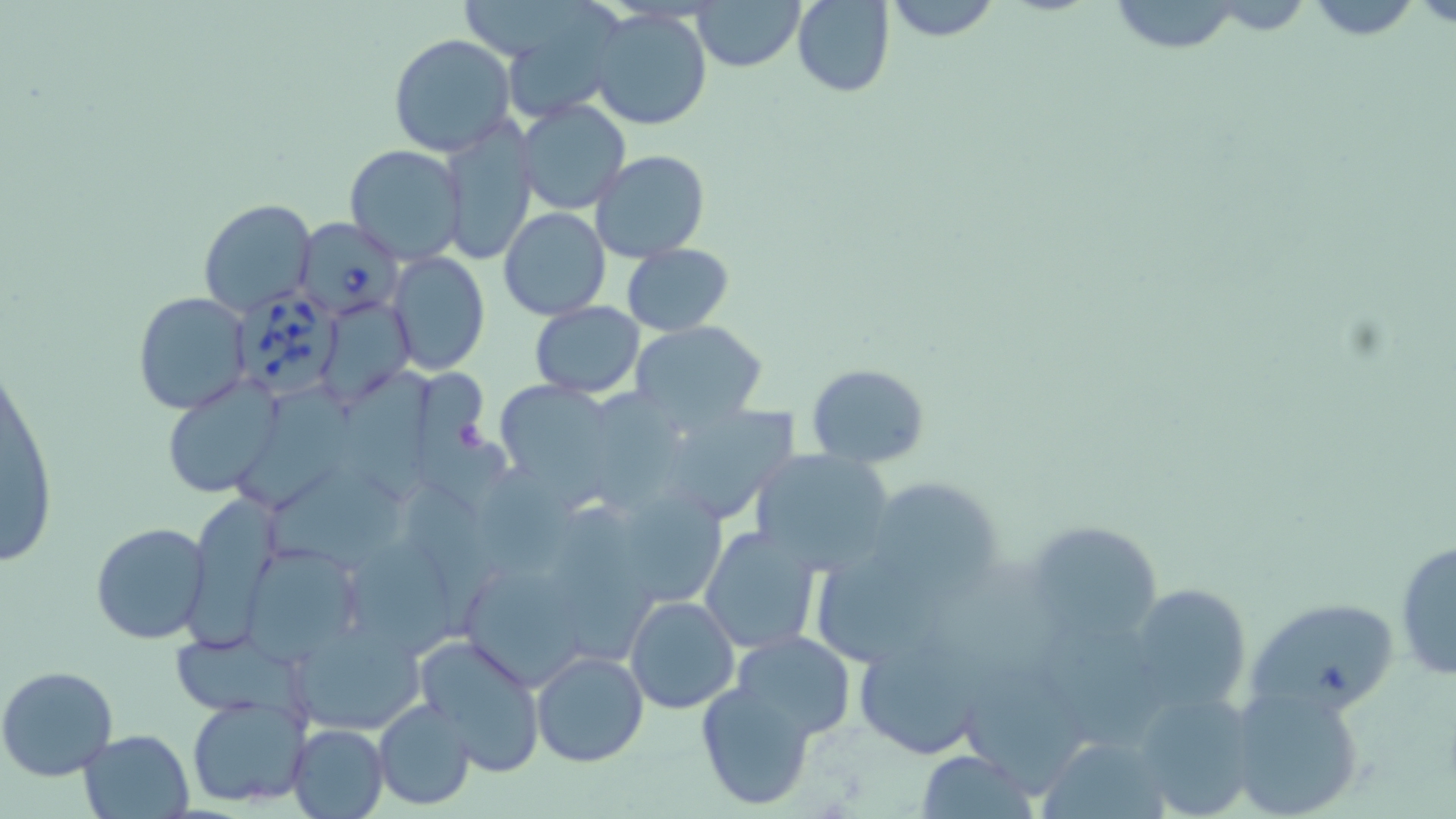
Approximate bounding boxes as named x1/y1/x2/y2 corners in pixels. Babesia divergens-infected red blood cell locations: (x1=297, y1=217, x2=404, y2=320), (x1=235, y1=287, x2=344, y2=400). Uninfected red blood cell locations: (x1=693, y1=0, x2=805, y2=71), (x1=793, y1=0, x2=895, y2=97), (x1=882, y1=0, x2=1000, y2=41), (x1=1104, y1=0, x2=1249, y2=56), (x1=1296, y1=0, x2=1438, y2=40), (x1=588, y1=7, x2=712, y2=131), (x1=515, y1=12, x2=628, y2=122), (x1=388, y1=34, x2=516, y2=157), (x1=516, y1=98, x2=632, y2=216), (x1=439, y1=117, x2=538, y2=267), (x1=345, y1=145, x2=466, y2=266), (x1=591, y1=150, x2=711, y2=261), (x1=198, y1=199, x2=317, y2=319), (x1=498, y1=206, x2=611, y2=320), (x1=622, y1=243, x2=734, y2=336), (x1=388, y1=251, x2=491, y2=375), (x1=133, y1=291, x2=252, y2=413), (x1=318, y1=295, x2=414, y2=408), (x1=528, y1=301, x2=646, y2=399), (x1=631, y1=321, x2=768, y2=428), (x1=2, y1=361, x2=60, y2=569), (x1=805, y1=362, x2=930, y2=467), (x1=420, y1=369, x2=523, y2=515), (x1=342, y1=372, x2=443, y2=507), (x1=491, y1=378, x2=618, y2=493), (x1=165, y1=380, x2=280, y2=498), (x1=245, y1=380, x2=352, y2=504), (x1=595, y1=389, x2=689, y2=517), (x1=671, y1=403, x2=804, y2=521), (x1=750, y1=448, x2=897, y2=574), (x1=267, y1=465, x2=417, y2=568), (x1=478, y1=465, x2=607, y2=587), (x1=868, y1=477, x2=1002, y2=594), (x1=405, y1=485, x2=502, y2=633), (x1=184, y1=490, x2=288, y2=647), (x1=568, y1=510, x2=667, y2=664), (x1=1021, y1=521, x2=1166, y2=644), (x1=90, y1=522, x2=211, y2=645), (x1=698, y1=526, x2=821, y2=656), (x1=346, y1=537, x2=462, y2=664), (x1=1394, y1=537, x2=1455, y2=683), (x1=237, y1=540, x2=366, y2=664), (x1=816, y1=545, x2=952, y2=668), (x1=468, y1=565, x2=587, y2=686), (x1=1127, y1=583, x2=1251, y2=715), (x1=625, y1=595, x2=739, y2=714), (x1=1247, y1=598, x2=1399, y2=717), (x1=294, y1=626, x2=428, y2=739), (x1=845, y1=628, x2=998, y2=762), (x1=731, y1=631, x2=857, y2=741), (x1=414, y1=635, x2=546, y2=776), (x1=173, y1=637, x2=321, y2=734), (x1=532, y1=649, x2=649, y2=768), (x1=965, y1=656, x2=1093, y2=797), (x1=0, y1=665, x2=119, y2=781), (x1=696, y1=680, x2=815, y2=810), (x1=1229, y1=681, x2=1368, y2=819), (x1=1128, y1=687, x2=1256, y2=819), (x1=186, y1=694, x2=312, y2=809), (x1=372, y1=698, x2=476, y2=809), (x1=287, y1=723, x2=390, y2=819), (x1=79, y1=729, x2=195, y2=818), (x1=1040, y1=734, x2=1172, y2=819), (x1=913, y1=751, x2=1039, y2=818). Slide-level diagnosis: Babesia divergens. Optical microscopy. Single field of view. Thin blood film. Image is 1456×819 pixels. Captured at 1000x magnification. May-Grünwald-Giemsa-stained preparation.